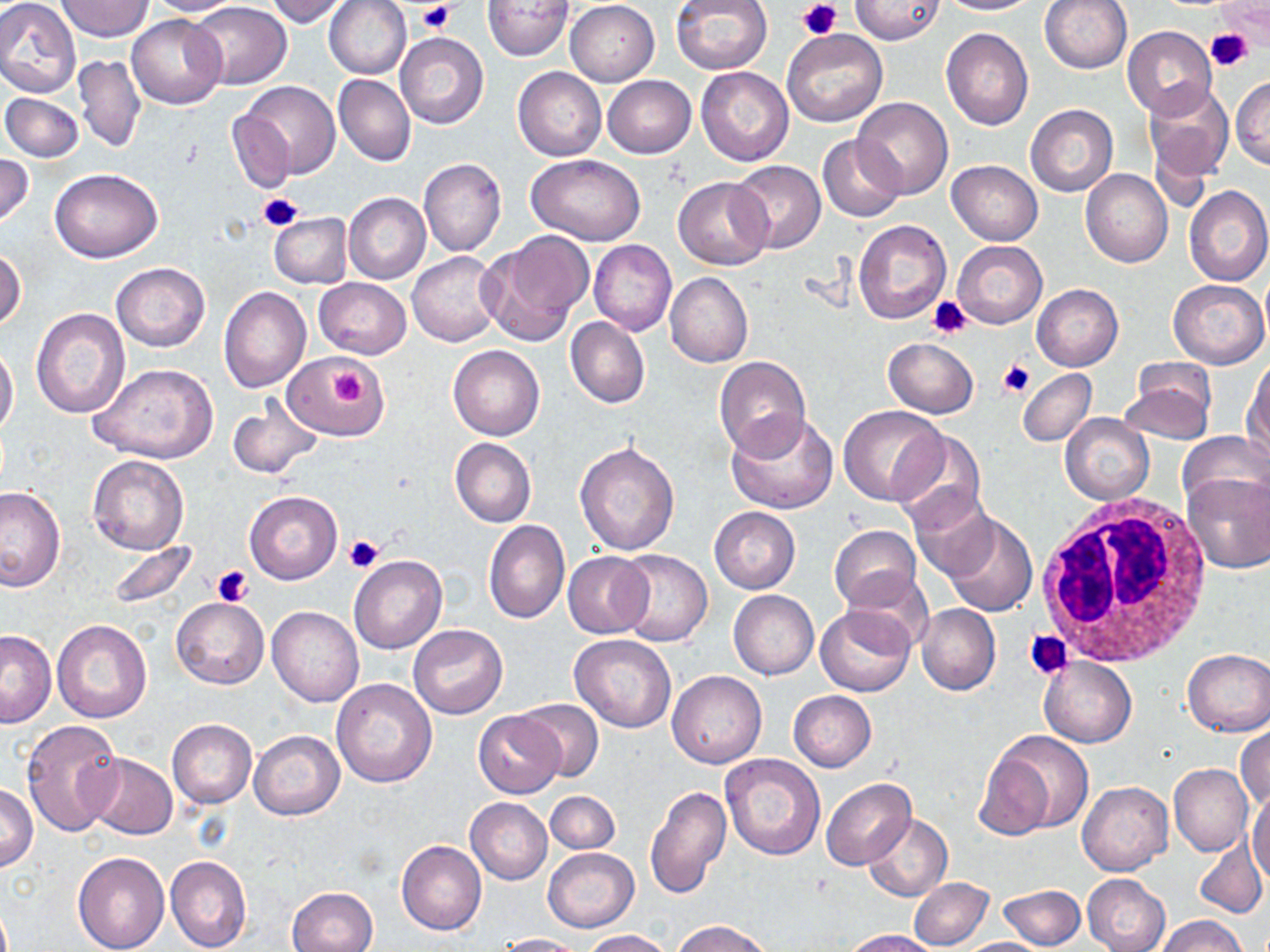
{
  "slide_level_diagnosis": "negative for blood parasites",
  "white_blood_cell_locations": "approximate bounding boxes as [x1, y1, x2, y2] in pixels: [1035, 495, 1215, 666]",
  "stain": "May-Grünwald-Giemsa",
  "preparation": "thin blood film",
  "platelet_locations": "approximate bounding boxes as [x1, y1, x2, y2] in pixels: [417, 1, 454, 35], [797, 1, 843, 40], [1205, 31, 1253, 72], [259, 192, 303, 230], [927, 296, 971, 336], [998, 358, 1035, 399], [329, 369, 371, 408], [342, 533, 385, 572], [211, 566, 253, 605], [1024, 631, 1072, 679]",
  "image_size": "1270×952 pixels",
  "modality": "optical microscopy",
  "uninfected_red_blood_cell_locations": "approximate bounding boxes as [x1, y1, x2, y2] in pixels: [0, 0, 81, 100], [56, 0, 152, 42], [145, 0, 247, 17], [264, 0, 351, 26], [324, 0, 411, 80], [670, 0, 773, 75], [850, 0, 945, 44], [938, 0, 1041, 15], [1040, 0, 1132, 74], [484, 1, 574, 60], [565, 1, 659, 86], [191, 2, 291, 90], [1214, 3, 1270, 49], [126, 14, 226, 109], [1122, 25, 1217, 118], [782, 28, 886, 126], [941, 28, 1034, 130], [395, 33, 488, 129], [74, 54, 147, 153], [513, 66, 605, 161], [696, 66, 794, 166], [333, 75, 416, 166], [602, 75, 696, 158], [1231, 77, 1270, 168], [239, 81, 340, 179], [1142, 82, 1234, 182], [2, 93, 82, 161], [852, 98, 952, 199], [1025, 104, 1118, 197], [228, 108, 298, 192], [818, 137, 905, 221], [0, 154, 34, 226], [528, 154, 645, 246], [418, 158, 506, 257], [730, 160, 825, 254], [947, 161, 1043, 244], [1080, 168, 1173, 268], [49, 169, 161, 263], [672, 177, 772, 270], [1183, 185, 1270, 287], [343, 193, 430, 285], [268, 212, 351, 288], [853, 220, 951, 324], [476, 234, 591, 347], [590, 240, 677, 336], [952, 242, 1047, 327], [0, 248, 25, 333], [407, 251, 503, 346], [111, 262, 209, 352], [665, 273, 753, 369], [314, 277, 411, 357], [1167, 279, 1268, 368], [1025, 285, 1108, 448], [1031, 285, 1122, 370], [219, 287, 311, 392], [31, 307, 130, 419], [566, 316, 649, 408], [883, 337, 978, 418], [0, 344, 18, 439], [448, 345, 545, 440], [288, 355, 388, 438], [714, 356, 811, 459], [1245, 358, 1270, 460], [88, 363, 218, 465], [1017, 368, 1096, 447], [1121, 370, 1215, 445], [228, 397, 322, 479], [838, 406, 948, 507], [726, 410, 839, 515], [1060, 412, 1154, 505], [891, 428, 987, 530], [1177, 431, 1269, 515], [449, 438, 536, 527], [574, 440, 680, 555], [87, 455, 189, 555], [1181, 471, 1270, 574], [0, 487, 65, 592], [243, 490, 343, 584], [910, 491, 997, 581], [709, 507, 800, 593], [939, 512, 1037, 616], [484, 520, 570, 624], [829, 525, 922, 611], [105, 540, 200, 613], [614, 549, 713, 646], [562, 551, 653, 639], [349, 556, 446, 653], [840, 570, 933, 651], [728, 590, 818, 679], [171, 597, 268, 689], [916, 603, 1000, 696], [815, 606, 916, 696], [267, 607, 363, 706], [51, 618, 153, 724], [408, 623, 507, 718], [0, 630, 57, 727], [569, 634, 677, 733], [1181, 649, 1270, 736], [1039, 657, 1136, 748], [668, 670, 767, 768], [331, 678, 438, 788], [787, 690, 876, 773], [515, 697, 603, 781], [474, 712, 564, 798], [167, 719, 256, 809], [21, 720, 123, 836], [1235, 725, 1269, 813], [248, 730, 344, 819], [983, 730, 1094, 836], [85, 752, 178, 839], [719, 753, 824, 858], [1169, 763, 1253, 856], [821, 778, 915, 869], [1077, 781, 1174, 875], [0, 784, 38, 871], [644, 786, 732, 902], [1247, 787, 1270, 884], [546, 791, 619, 853], [466, 798, 552, 883], [863, 813, 952, 901], [1192, 836, 1267, 918], [397, 841, 486, 934], [544, 848, 638, 930], [73, 850, 170, 952], [165, 855, 251, 952], [1082, 873, 1171, 952], [909, 877, 993, 950], [997, 883, 1086, 949], [288, 886, 378, 952], [1155, 915, 1249, 952], [673, 920, 773, 952], [581, 929, 674, 952], [843, 929, 940, 952], [496, 933, 583, 951], [957, 937, 1050, 952]",
  "field_of_view": "one of a larger specimen",
  "magnification": "1000x"
}